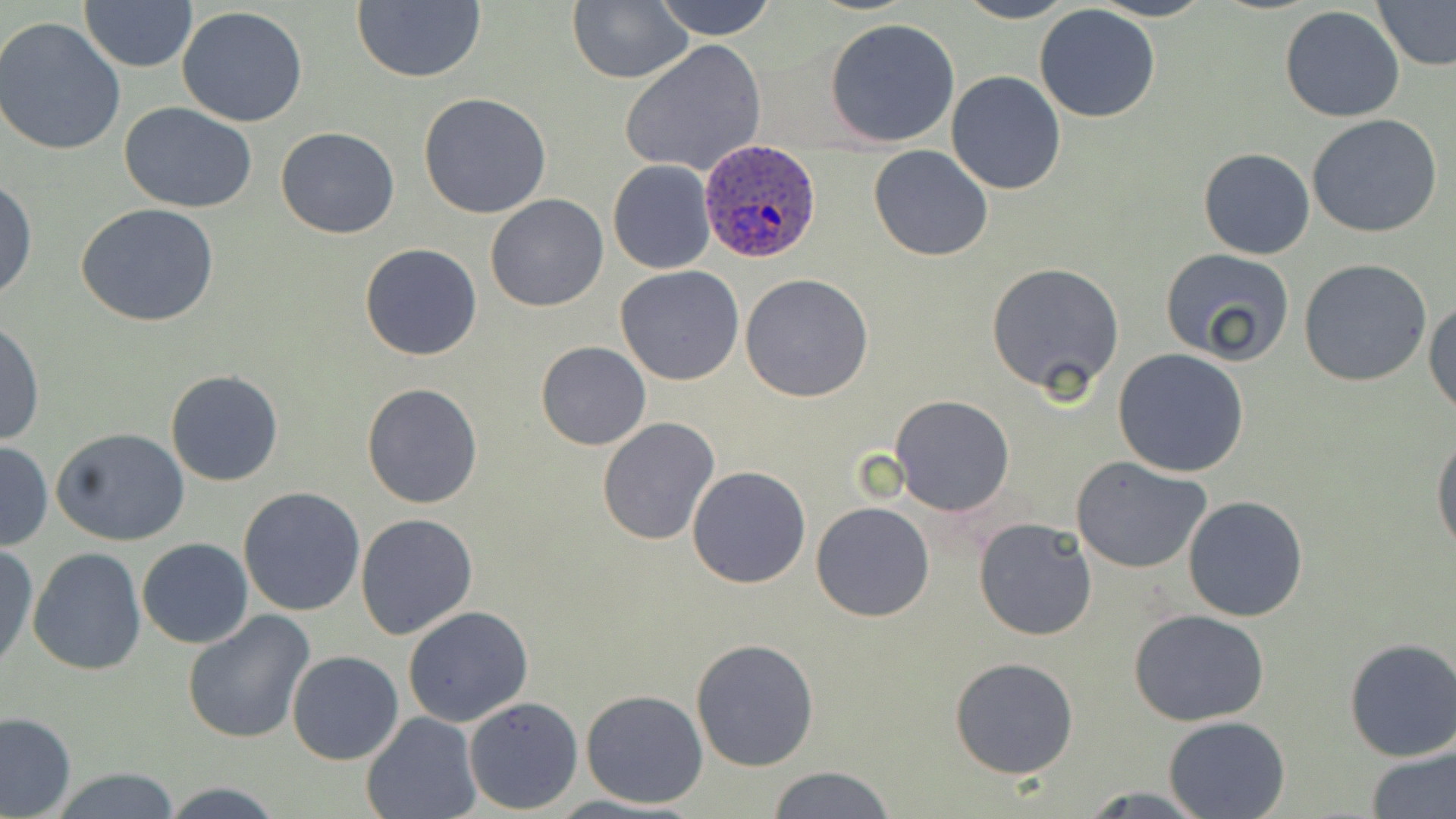
Approximate bounding boxes as [x1, y1, x2, y2] in pixels. Uninfected red blood cell locations: [569, 0, 693, 85], [647, 0, 780, 40], [954, 0, 1078, 24], [1089, 0, 1212, 22], [1375, 1, 1456, 69], [80, 2, 198, 72], [350, 2, 487, 84], [1033, 5, 1162, 125], [177, 6, 309, 128], [1278, 7, 1406, 124], [825, 18, 960, 147], [0, 19, 126, 156], [620, 41, 766, 178], [946, 72, 1067, 193], [418, 93, 552, 218], [118, 103, 261, 216], [1306, 115, 1444, 239], [275, 126, 400, 239], [868, 145, 995, 261], [1198, 148, 1317, 260], [607, 159, 716, 275], [1, 176, 37, 304], [485, 194, 609, 312], [76, 202, 220, 327], [359, 243, 482, 360], [1159, 248, 1297, 364], [1300, 258, 1433, 388], [986, 263, 1128, 398], [615, 264, 745, 386], [740, 273, 874, 402], [1425, 297, 1456, 418], [1, 320, 43, 449], [537, 342, 651, 449], [1113, 348, 1249, 477], [165, 369, 284, 487], [361, 382, 483, 508], [889, 395, 1016, 516], [596, 417, 720, 545], [53, 427, 190, 547], [1430, 429, 1456, 556], [0, 441, 51, 551], [1070, 455, 1212, 573], [687, 465, 812, 588], [238, 486, 365, 615], [1181, 495, 1309, 623], [810, 501, 935, 622], [354, 514, 478, 642], [974, 517, 1097, 641], [137, 537, 253, 649], [0, 543, 37, 671], [27, 548, 147, 676], [402, 606, 534, 728], [1128, 607, 1274, 728], [182, 610, 314, 744], [690, 638, 819, 771], [1343, 638, 1456, 762], [287, 650, 405, 765], [950, 656, 1079, 779], [580, 689, 709, 810], [463, 696, 582, 812], [0, 711, 75, 818], [362, 712, 480, 819], [1163, 715, 1290, 818], [1367, 747, 1456, 817], [764, 765, 897, 819], [45, 767, 187, 819], [160, 783, 285, 818]. Plasmodium ovale-infected red blood cell locations: [699, 140, 822, 265]. Slide-level diagnosis: Plasmodium ovale. Captured at 1000x magnification. Thin blood film. May-Grünwald-Giemsa stain. One field of a larger specimen. Image is 1456×819 pixels. Optical microscopy.